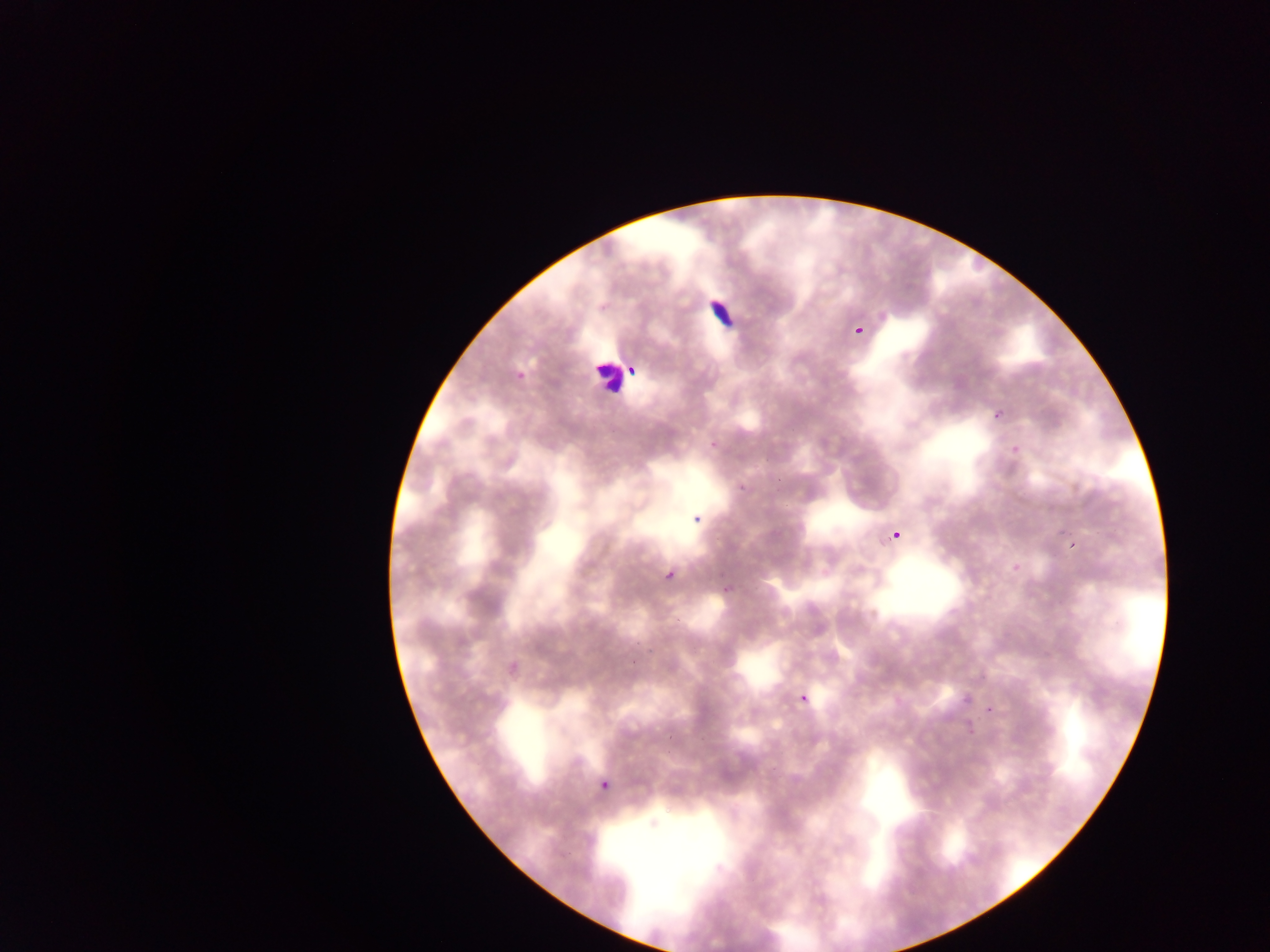
Approximate bounding boxes as {left, top, right, bottom} in pixels. Malaria parasite locations: {854, 323, 868, 336}, {629, 366, 639, 378}, {514, 369, 527, 381}, {985, 401, 1014, 422}, {734, 483, 747, 498}, {687, 508, 700, 525}, {885, 518, 903, 543}, {1068, 541, 1078, 552}, {662, 568, 677, 583}, {719, 585, 731, 602}, {798, 694, 810, 706}, {986, 706, 997, 715}, {598, 769, 607, 798}. Leukocyte locations: {701, 289, 741, 330}, {590, 357, 625, 397}. Collected in Ghana. One field of view. Thin blood film. Image is 1270×952 pixels. Mobile-phone photograph taken through the microscope.